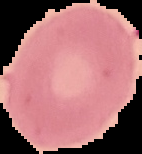
result = no Plasmodium parasites seen
preparation = thin blood smear
image size = 142×154 pixels
image type = segmented cell region with the area outside set to black